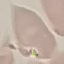
Summary:
  - Malaria status: uninfected
  - Image type: cell patch, automatically extracted from a larger field of view and resized to 64 × 64 pixels
  - Stain: Giemsa
  - Capture: smartphone through the microscope eyepiece
  - Preparation: thin blood smear